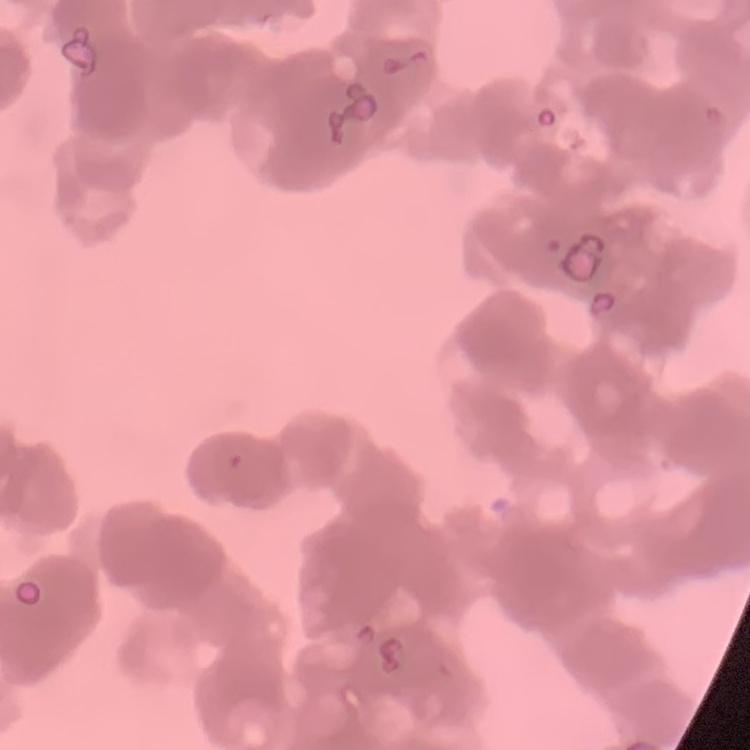

The erythrocytes show rouleaux formation. Square crop of a larger photomicrograph. Stained with either Field's or Giemsa. Thin blood film.